Comment on the morphology of the red blood cells.
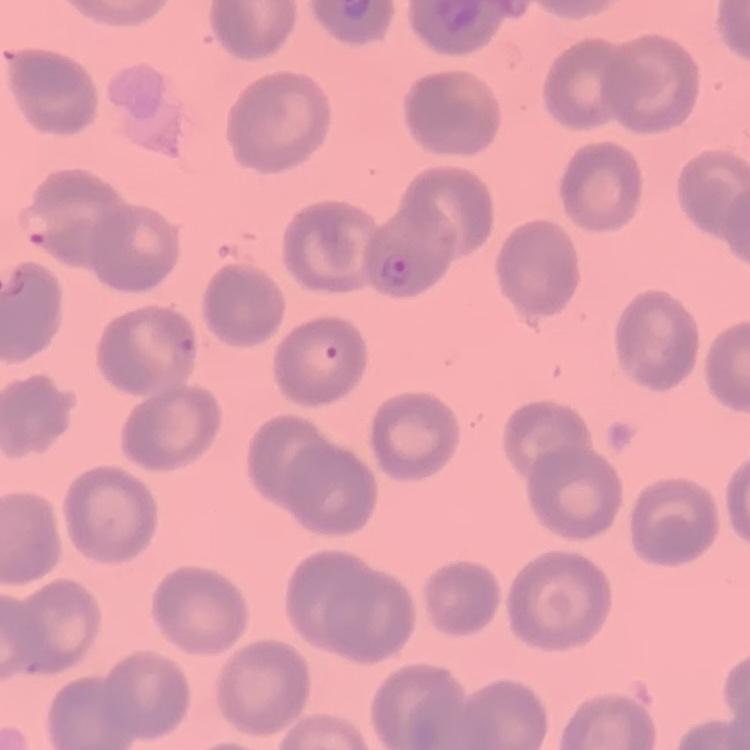
No rouleaux formation.

image_type: square crop of a larger photomicrograph
stain: Field's or Giemsa
preparation: thin blood film